Outline each blood parasite and name the species.
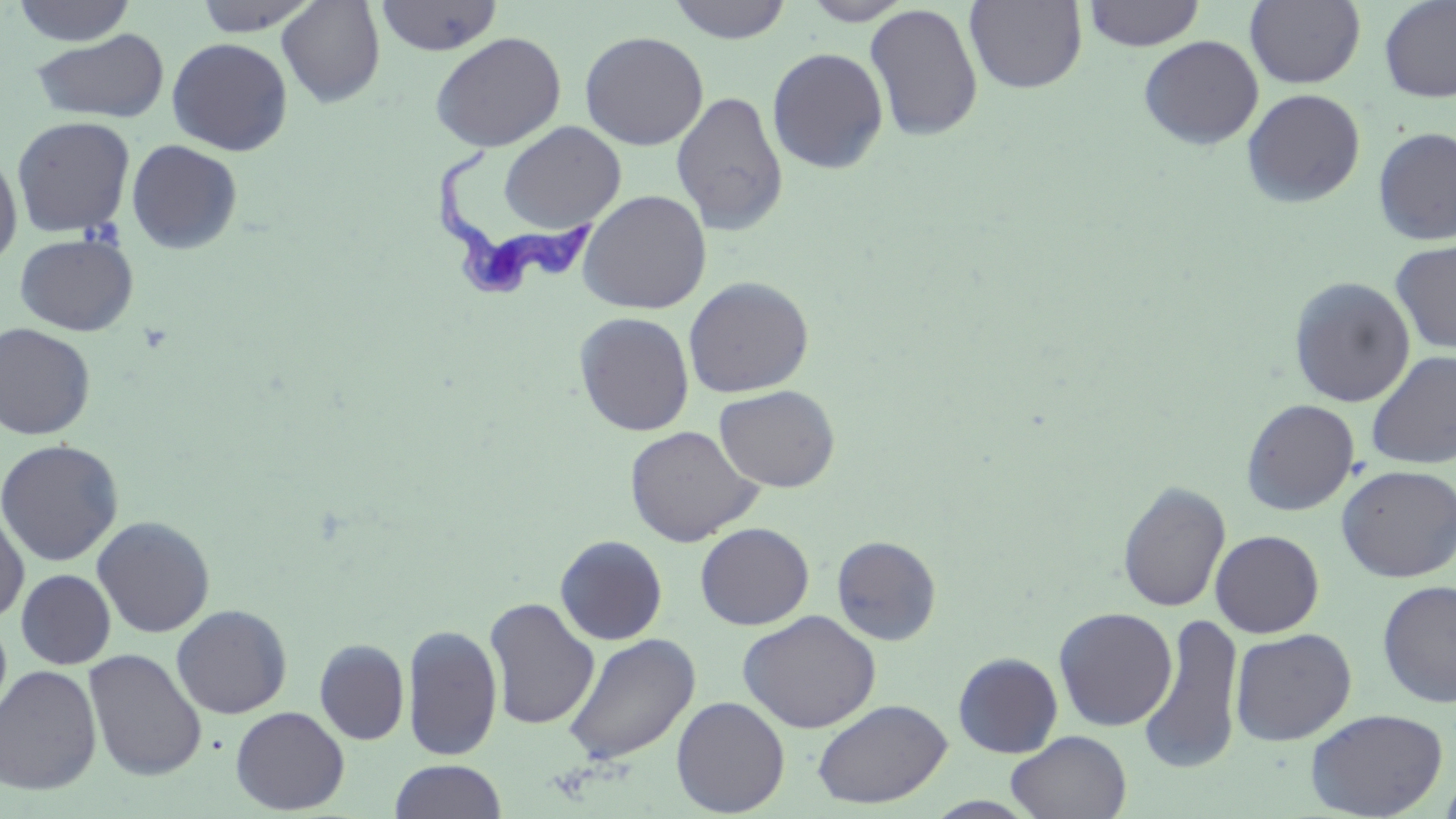
Approximate bounding boxes as (x1, y1, x2, y2) in pixels.
Trypanosoma brucei: (432, 149, 604, 305).
No Plasmodium falciparum, Plasmodium ovale, Plasmodium malariae, Plasmodium vivax, or Babesia divergens observed.

slide-level diagnosis = Trypanosoma brucei
modality = light microscopy
uninfected red blood cell locations = approximate bounding boxes as (x1, y1, x2, y2) in pixels: (12, 0, 136, 46), (193, 0, 323, 36), (276, 0, 386, 108), (374, 0, 503, 56), (666, 0, 793, 44), (801, 0, 915, 25), (1082, 0, 1205, 51), (1245, 0, 1365, 88), (1378, 0, 1456, 103), (964, 1, 1088, 93), (864, 3, 983, 142), (31, 28, 170, 124), (579, 30, 709, 150), (430, 32, 567, 152), (1138, 35, 1264, 150), (166, 37, 293, 156), (767, 47, 889, 174), (1242, 88, 1366, 208), (670, 89, 789, 235), (12, 115, 136, 238), (498, 121, 626, 234), (1372, 126, 1456, 246), (126, 139, 243, 255), (0, 149, 22, 268), (577, 190, 712, 315), (15, 233, 138, 336), (1391, 239, 1456, 354), (683, 276, 815, 398), (1288, 277, 1416, 408), (574, 311, 695, 436), (0, 322, 96, 440), (1365, 351, 1456, 470), (714, 385, 840, 492), (1241, 398, 1359, 515), (624, 425, 763, 547), (0, 439, 124, 566), (1336, 464, 1456, 582), (1117, 480, 1231, 613), (0, 505, 29, 625), (91, 515, 216, 638), (695, 522, 814, 630), (1210, 529, 1324, 638), (555, 534, 668, 645), (831, 535, 942, 646), (16, 569, 115, 669), (1376, 579, 1456, 709), (483, 597, 599, 730), (171, 604, 292, 719), (1053, 607, 1178, 731), (737, 610, 881, 734), (1139, 612, 1244, 776), (0, 614, 12, 727), (401, 623, 503, 761), (1230, 628, 1356, 745), (562, 632, 700, 766), (314, 638, 409, 745), (83, 648, 207, 781), (953, 652, 1063, 758), (0, 664, 102, 797), (671, 696, 790, 817), (811, 698, 951, 809), (230, 706, 349, 815), (1305, 708, 1448, 818), (1006, 731, 1131, 818), (390, 760, 506, 818), (1439, 768, 1456, 818)
field of view = single
stain = May-Grünwald-Giemsa
preparation = thin blood film
image size = 1456×819 pixels
magnification = 1000x